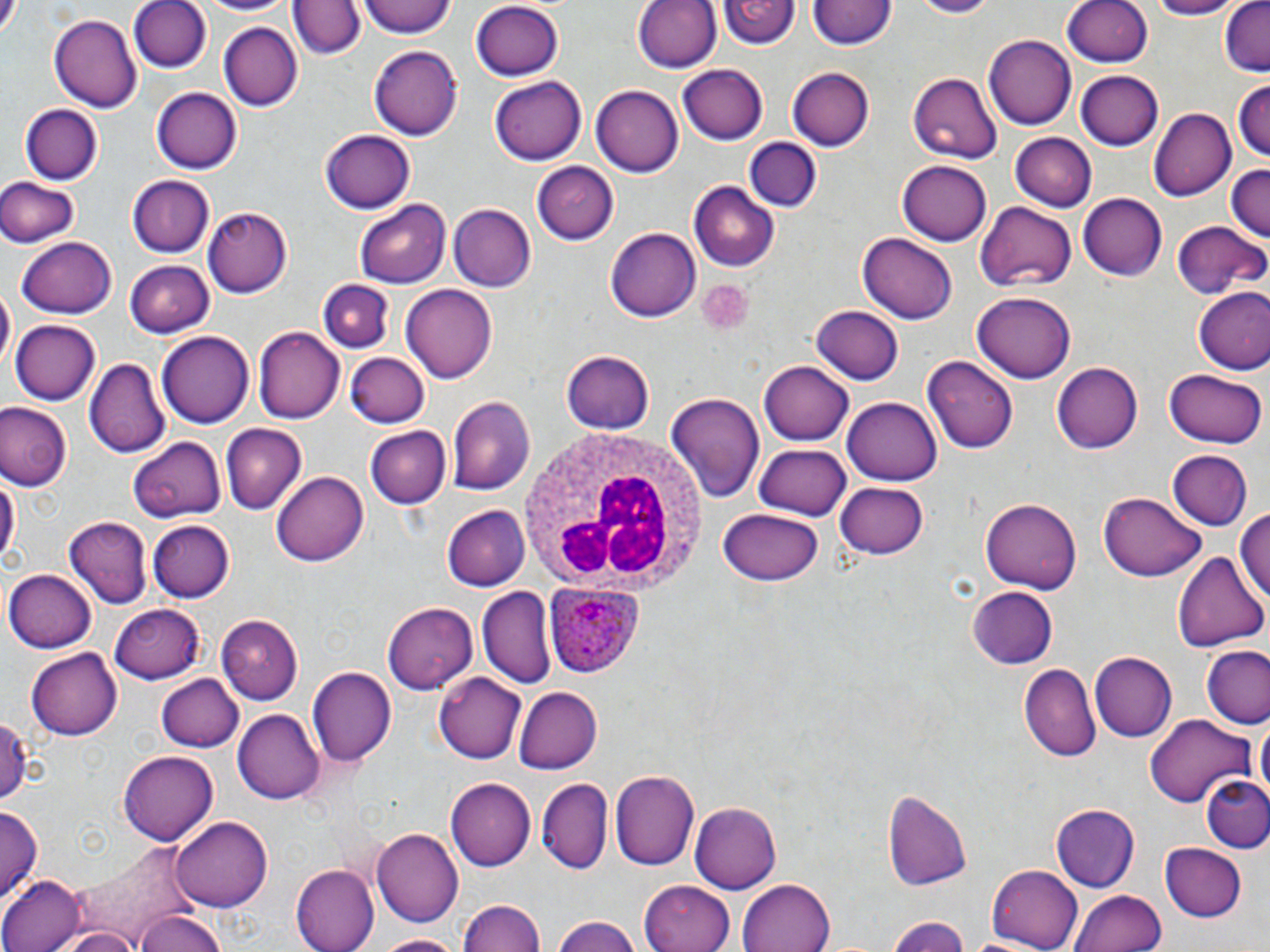
slide-level diagnosis = Plasmodium ovale
modality = optical microscopy
white blood cell locations = approximate bounding boxes as named x1/y1/x2/y2 corners in pixels: (x1=513, y1=423, x2=705, y2=594)
uninfected red blood cell locations = approximate bounding boxes as named x1/y1/x2/y2 corners in pixels: (x1=127, y1=0, x2=209, y2=74), (x1=192, y1=0, x2=299, y2=17), (x1=359, y1=0, x2=457, y2=39), (x1=632, y1=0, x2=719, y2=73), (x1=912, y1=0, x2=998, y2=18), (x1=1058, y1=0, x2=1155, y2=69), (x1=1146, y1=0, x2=1239, y2=19), (x1=1218, y1=0, x2=1270, y2=76), (x1=290, y1=1, x2=364, y2=62), (x1=720, y1=1, x2=796, y2=53), (x1=808, y1=1, x2=894, y2=53), (x1=471, y1=2, x2=564, y2=80), (x1=47, y1=12, x2=142, y2=113), (x1=220, y1=22, x2=303, y2=112), (x1=983, y1=35, x2=1076, y2=131), (x1=367, y1=45, x2=463, y2=141), (x1=678, y1=63, x2=767, y2=145), (x1=787, y1=67, x2=875, y2=151), (x1=1075, y1=69, x2=1162, y2=150), (x1=907, y1=72, x2=1004, y2=164), (x1=488, y1=76, x2=586, y2=166), (x1=1233, y1=79, x2=1269, y2=168), (x1=591, y1=85, x2=685, y2=177), (x1=151, y1=87, x2=242, y2=174), (x1=19, y1=103, x2=102, y2=183), (x1=1151, y1=107, x2=1235, y2=202), (x1=320, y1=130, x2=415, y2=213), (x1=1009, y1=133, x2=1097, y2=212), (x1=743, y1=136, x2=822, y2=213), (x1=897, y1=158, x2=991, y2=245), (x1=530, y1=162, x2=619, y2=246), (x1=1224, y1=163, x2=1270, y2=243), (x1=128, y1=174, x2=214, y2=258), (x1=0, y1=177, x2=80, y2=247), (x1=689, y1=183, x2=780, y2=272), (x1=1076, y1=193, x2=1166, y2=280), (x1=356, y1=198, x2=451, y2=287), (x1=978, y1=200, x2=1076, y2=292), (x1=449, y1=203, x2=536, y2=292), (x1=203, y1=206, x2=291, y2=295), (x1=1173, y1=218, x2=1266, y2=301), (x1=606, y1=226, x2=701, y2=321), (x1=858, y1=233, x2=958, y2=323), (x1=18, y1=235, x2=117, y2=316), (x1=125, y1=260, x2=214, y2=338), (x1=317, y1=277, x2=393, y2=351), (x1=402, y1=282, x2=498, y2=381), (x1=1193, y1=287, x2=1270, y2=375), (x1=974, y1=290, x2=1074, y2=382), (x1=808, y1=303, x2=904, y2=386), (x1=10, y1=317, x2=100, y2=403), (x1=255, y1=326, x2=343, y2=425), (x1=156, y1=332, x2=255, y2=429), (x1=562, y1=350, x2=654, y2=435), (x1=345, y1=353, x2=430, y2=427), (x1=924, y1=355, x2=1021, y2=453), (x1=86, y1=359, x2=170, y2=458), (x1=762, y1=361, x2=853, y2=446), (x1=1053, y1=362, x2=1143, y2=453), (x1=1165, y1=369, x2=1263, y2=447), (x1=664, y1=393, x2=764, y2=502), (x1=448, y1=394, x2=535, y2=494), (x1=842, y1=396, x2=942, y2=486), (x1=0, y1=403, x2=71, y2=491), (x1=221, y1=424, x2=305, y2=515), (x1=363, y1=426, x2=450, y2=510), (x1=130, y1=435, x2=227, y2=521), (x1=754, y1=440, x2=852, y2=520), (x1=1168, y1=451, x2=1252, y2=530), (x1=0, y1=468, x2=17, y2=573), (x1=272, y1=470, x2=368, y2=567), (x1=836, y1=479, x2=929, y2=559), (x1=1096, y1=491, x2=1205, y2=582), (x1=983, y1=496, x2=1083, y2=590), (x1=441, y1=505, x2=530, y2=591), (x1=1233, y1=507, x2=1270, y2=610), (x1=717, y1=508, x2=823, y2=587), (x1=59, y1=515, x2=149, y2=609), (x1=147, y1=519, x2=234, y2=603), (x1=1172, y1=551, x2=1265, y2=653), (x1=6, y1=569, x2=98, y2=652), (x1=967, y1=585, x2=1056, y2=668), (x1=477, y1=586, x2=557, y2=688), (x1=383, y1=602, x2=480, y2=691), (x1=109, y1=604, x2=204, y2=682), (x1=217, y1=616, x2=303, y2=704), (x1=1204, y1=646, x2=1270, y2=731), (x1=26, y1=647, x2=120, y2=740), (x1=1090, y1=653, x2=1176, y2=743), (x1=1020, y1=663, x2=1099, y2=761), (x1=309, y1=666, x2=396, y2=766), (x1=434, y1=672, x2=527, y2=765), (x1=156, y1=673, x2=242, y2=753), (x1=515, y1=686, x2=603, y2=773), (x1=233, y1=710, x2=325, y2=804), (x1=0, y1=712, x2=34, y2=809), (x1=1144, y1=713, x2=1258, y2=808), (x1=1254, y1=717, x2=1270, y2=806), (x1=118, y1=750, x2=217, y2=844), (x1=612, y1=770, x2=698, y2=872), (x1=1202, y1=776, x2=1270, y2=853), (x1=446, y1=779, x2=536, y2=871), (x1=537, y1=779, x2=613, y2=873), (x1=1187, y1=780, x2=1268, y2=915), (x1=884, y1=788, x2=972, y2=891), (x1=689, y1=802, x2=782, y2=894), (x1=1053, y1=804, x2=1139, y2=893), (x1=0, y1=806, x2=42, y2=904), (x1=172, y1=815, x2=270, y2=912), (x1=372, y1=830, x2=463, y2=927), (x1=76, y1=842, x2=200, y2=943), (x1=1159, y1=844, x2=1246, y2=923), (x1=988, y1=863, x2=1085, y2=952), (x1=294, y1=864, x2=381, y2=952), (x1=0, y1=877, x2=82, y2=952), (x1=738, y1=878, x2=835, y2=952), (x1=640, y1=880, x2=736, y2=952), (x1=1071, y1=888, x2=1173, y2=952), (x1=459, y1=897, x2=544, y2=952), (x1=133, y1=911, x2=230, y2=952), (x1=550, y1=914, x2=645, y2=952), (x1=887, y1=914, x2=972, y2=952), (x1=54, y1=925, x2=142, y2=952), (x1=374, y1=933, x2=470, y2=951)
field of view = single
magnification = 1000x
preparation = thin blood film
stain = May-Grünwald-Giemsa
image size = 1270×952 pixels
Plasmodium ovale-infected red blood cell locations = approximate bounding boxes as named x1/y1/x2/y2 corners in pixels: (x1=548, y1=584, x2=643, y2=679)